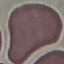
Summary:
  - Result: no malaria parasites detected
  - Preparation: thin blood smear
  - Capture: smartphone camera at the microscope eyepiece
  - Stain: Giemsa
  - Image type: automatically extracted cell patch, resized to 64 × 64 pixels